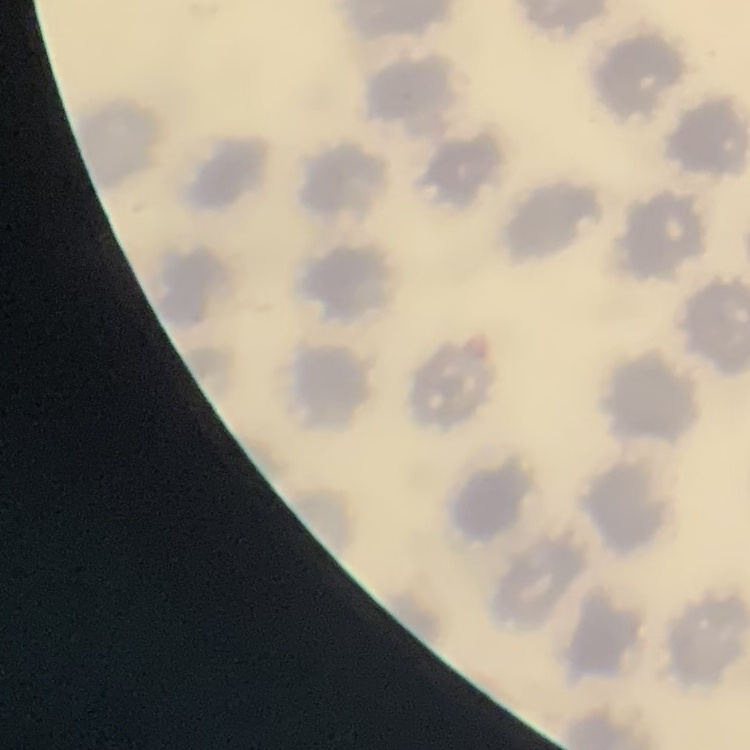
Summary:
  - Red blood cell morphology: no rouleaux formation
  - Preparation: thin blood smear
  - Image type: one tile cut from a larger photomicrograph
  - Stain: Field's or Giemsa